Assess this cell for malaria.
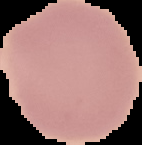
It is uninfected.

Summary:
  - Image type: segmented cell region with the area outside set to black
  - Preparation: thin blood film
  - Image size: 142×145 pixels